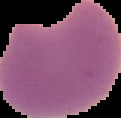
Summary:
  - Preparation: thin blood smear
  - Result: malaria parasites detected
  - Image size: 121×118 pixels
  - Image type: segmented cell region with the area outside set to black